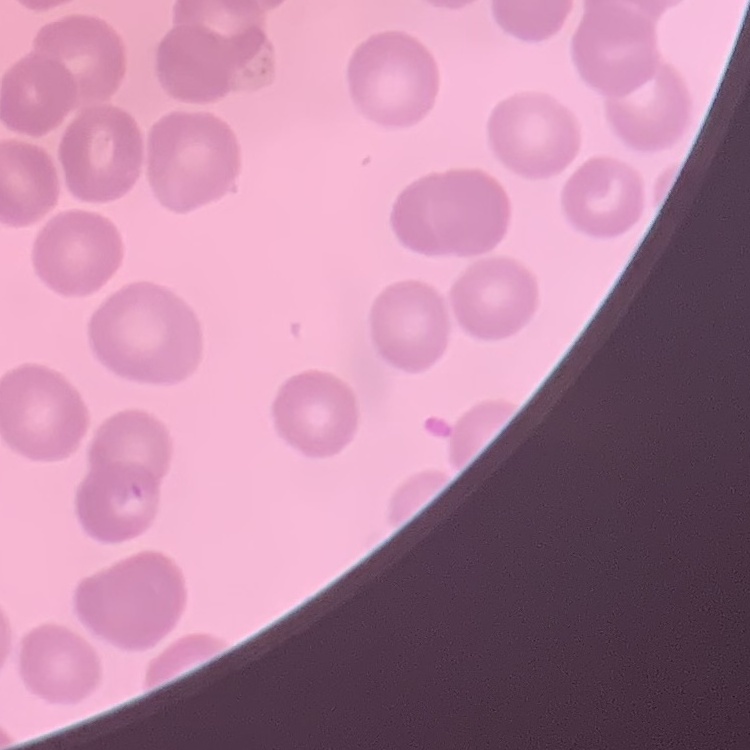

Summary:
  - Erythrocyte morphology: no rouleaux formation
  - Stain: Field's or Giemsa
  - Preparation: thin blood smear
  - Image type: one tile cut from a larger photomicrograph